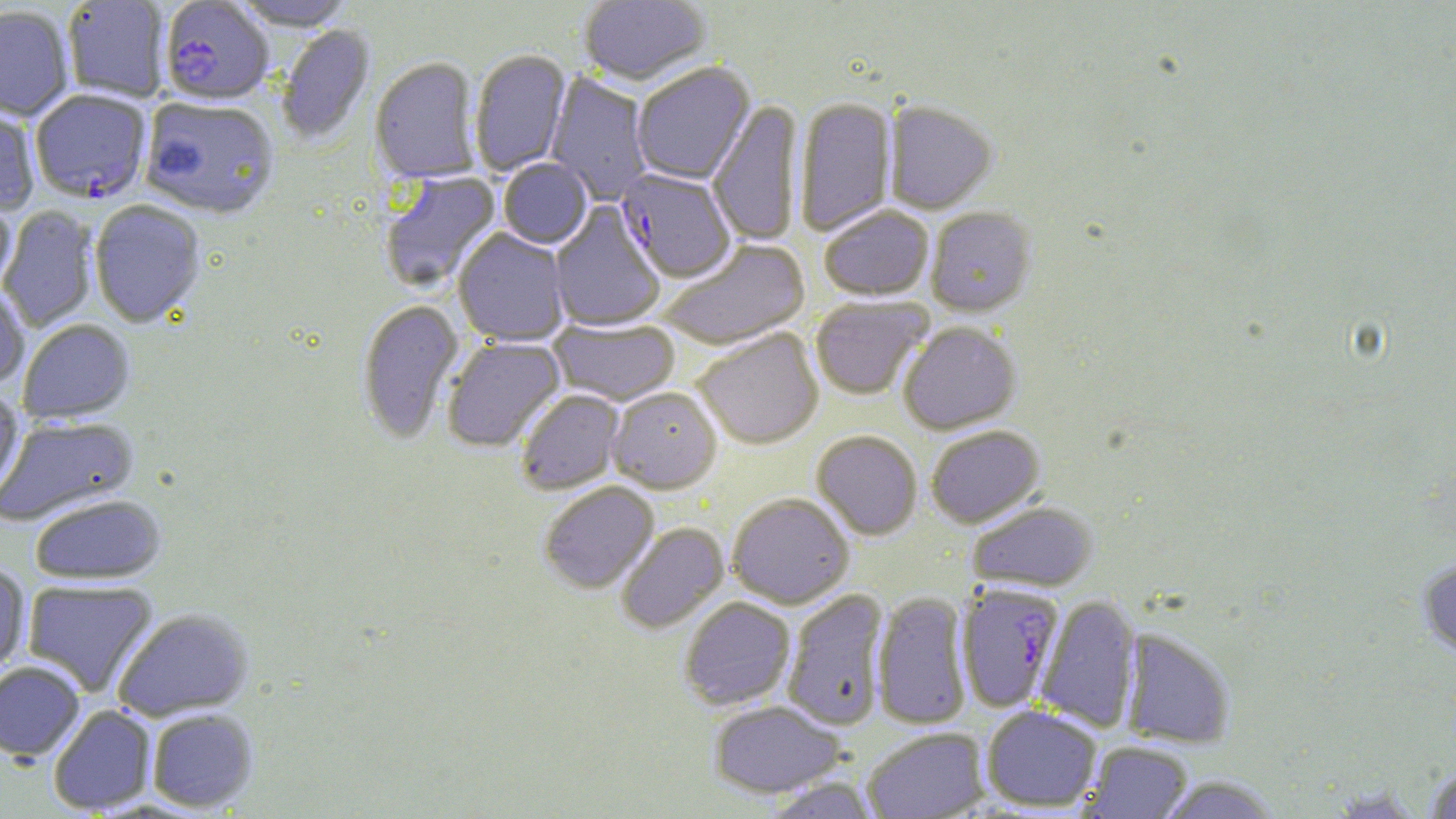
Summary:
  - Coordinate format: approximate bounding boxes as (x1, y1, x2, y2) in pixels
  - Plasmodium falciparum-infected red blood cell locations: (159, 2, 274, 108), (30, 91, 152, 205), (616, 170, 736, 284), (956, 583, 1064, 712)
  - Uninfected red blood cell locations: (579, 0, 711, 88), (63, 1, 169, 103), (230, 1, 356, 33), (0, 7, 74, 122), (277, 26, 376, 148), (469, 50, 571, 177), (370, 58, 482, 186), (632, 64, 756, 186), (545, 72, 653, 206), (139, 98, 281, 221), (795, 98, 897, 236), (0, 100, 40, 216), (708, 101, 803, 246), (884, 102, 997, 215), (498, 160, 592, 251), (380, 172, 503, 294), (0, 191, 17, 294), (90, 202, 205, 329), (550, 202, 665, 333), (0, 206, 100, 333), (819, 207, 934, 302), (925, 208, 1036, 318), (453, 228, 570, 347), (658, 239, 811, 351), (0, 285, 30, 391), (810, 296, 932, 401), (357, 300, 464, 446), (548, 319, 681, 407), (19, 320, 135, 424), (898, 323, 1021, 435), (693, 329, 824, 450), (442, 337, 566, 453), (0, 386, 25, 505), (608, 388, 723, 494), (515, 390, 625, 495), (0, 416, 139, 527), (926, 425, 1045, 528), (811, 431, 922, 541), (539, 482, 659, 595), (727, 493, 854, 609), (30, 495, 167, 585), (967, 501, 1098, 592), (615, 522, 730, 634), (1417, 557, 1456, 659), (0, 563, 31, 678), (22, 580, 158, 697), (782, 588, 890, 730), (872, 591, 972, 730), (1036, 595, 1141, 732), (679, 597, 796, 711), (113, 609, 253, 720), (1121, 629, 1235, 748), (0, 662, 85, 761), (708, 699, 845, 798), (982, 705, 1102, 812), (48, 706, 156, 815), (147, 709, 257, 812), (862, 726, 990, 818), (1083, 741, 1193, 818), (1424, 763, 1456, 819), (1157, 775, 1283, 818), (759, 777, 882, 818)
  - Slide-level diagnosis: Plasmodium falciparum
  - Image size: 1456×819 pixels
  - Preparation: thin blood film
  - Modality: light microscopy
  - Stain: May-Grünwald-Giemsa
  - Field of view: single
  - Magnification: 1000x